Identify the parasite.
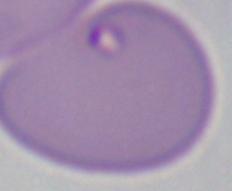
Babesia.

magnification = 1000x
modality = micrograph